Assess this cell for malaria.
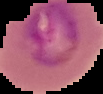
It is parasitized.

Summary:
  - Image type: segmented cell region with the area outside set to black
  - Image size: 103×94 pixels
  - Preparation: thin blood film